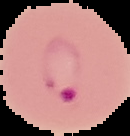

malaria status = parasitized
image size = 130×136 pixels
preparation = thin blood film
image type = segmented cell region on a black background